Comment on the morphology of the red blood cells.
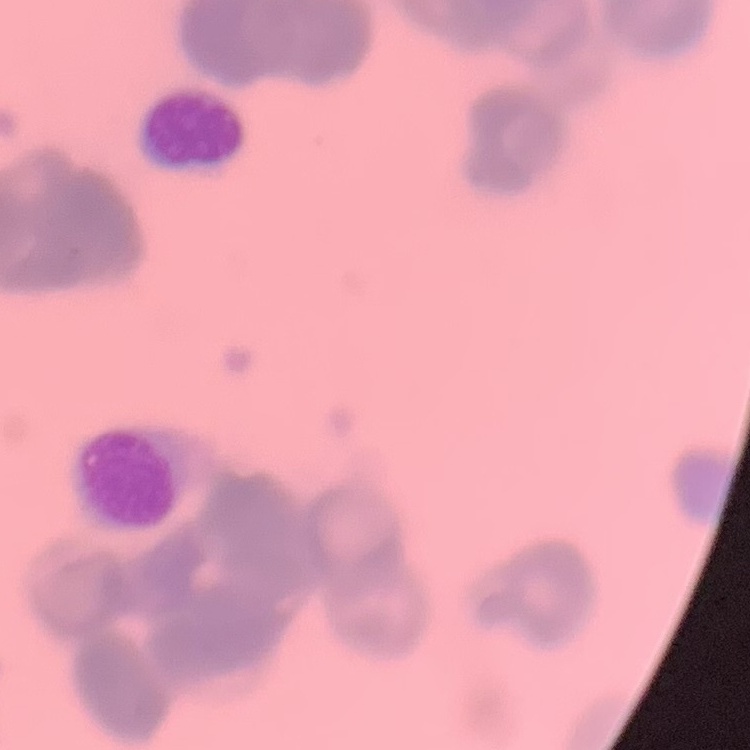
Rouleaux formation.

One tile cut from a larger photomicrograph. Field's or Giemsa stain. Thin peripheral smear.